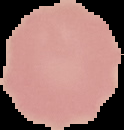
Summary:
  - Preparation: thin blood smear
  - Result: no malaria parasites detected
  - Image size: 124×130 pixels
  - Image type: cell region segmented out of the field of view; surrounding area masked to black